Evaluate for Plasmodium parasites.
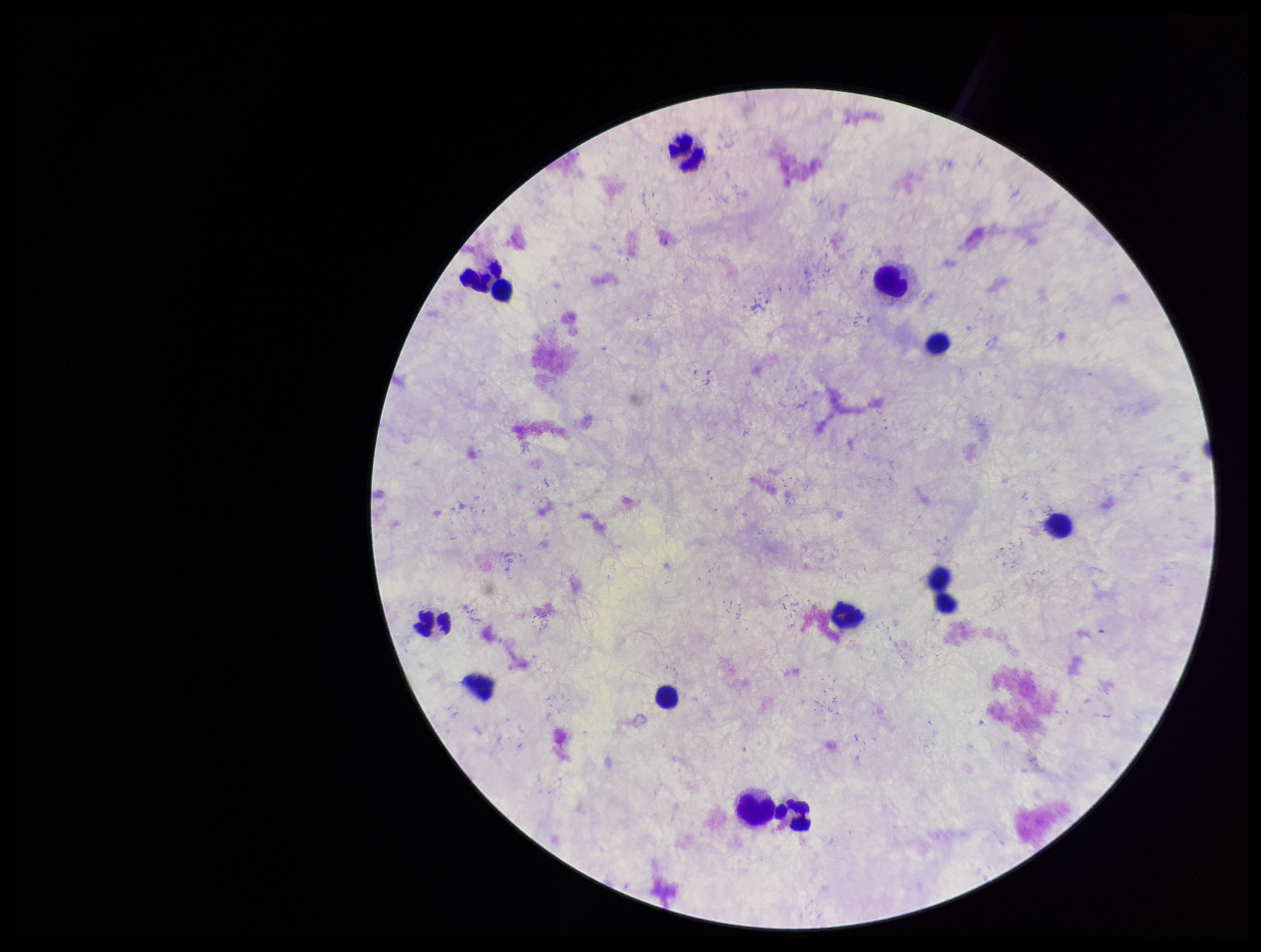
None detected.

Summary:
  - Preparation: thick blood smear
  - Capture: smartphone photograph through the microscope eyepiece
  - Patient malaria status: negative
  - Leukocyte count: 12
  - Stain: Giemsa
  - Image size: 1261×952 pixels
  - Field of view: one from this slide
  - Parasite count: 0